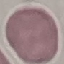
result = no malaria parasites detected
image type = automatically extracted cell patch, resized to 64 × 64 pixels
stain = Giemsa
capture = smartphone through the microscope eyepiece
preparation = thin blood smear